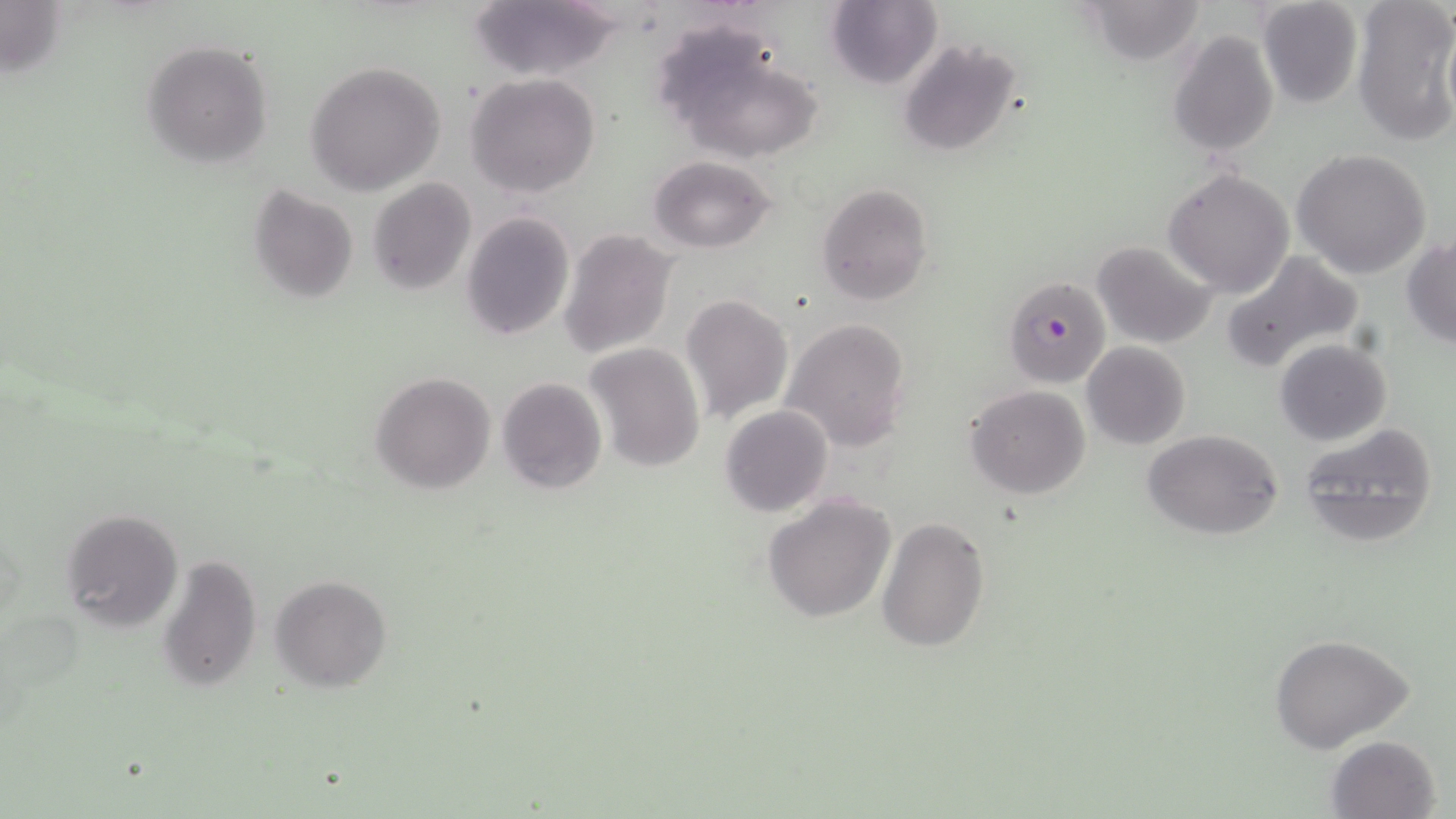
Plasmodium falciparum-infected red blood cell locations = approximate bounding boxes as named x1/y1/x2/y2 corners in pixels: (x1=1002, y1=277, x2=1111, y2=389)
slide-level diagnosis = Plasmodium falciparum
image size = 1456×819 pixels
field of view = one of a larger specimen
preparation = thin blood film
magnification = 1000x
modality = optical microscopy
stain = May-Grünwald-Giemsa
uninfected red blood cell locations = approximate bounding boxes as named x1/y1/x2/y2 corners in pixels: (x1=467, y1=0, x2=624, y2=82), (x1=1080, y1=0, x2=1209, y2=66), (x1=1352, y1=0, x2=1456, y2=147), (x1=826, y1=1, x2=943, y2=89), (x1=1257, y1=1, x2=1364, y2=109), (x1=651, y1=23, x2=824, y2=164), (x1=1168, y1=28, x2=1279, y2=156), (x1=896, y1=36, x2=1024, y2=157), (x1=140, y1=40, x2=273, y2=168), (x1=305, y1=60, x2=446, y2=195), (x1=466, y1=73, x2=600, y2=198), (x1=1293, y1=149, x2=1432, y2=280), (x1=650, y1=155, x2=776, y2=253), (x1=1163, y1=167, x2=1296, y2=298), (x1=367, y1=178, x2=477, y2=294), (x1=815, y1=182, x2=934, y2=306), (x1=248, y1=185, x2=359, y2=303), (x1=461, y1=211, x2=574, y2=340), (x1=559, y1=229, x2=677, y2=359), (x1=1403, y1=235, x2=1456, y2=346), (x1=1091, y1=239, x2=1217, y2=348), (x1=1219, y1=250, x2=1362, y2=375), (x1=680, y1=293, x2=794, y2=426), (x1=782, y1=317, x2=912, y2=452), (x1=1273, y1=339, x2=1392, y2=446), (x1=1082, y1=342, x2=1191, y2=450), (x1=585, y1=343, x2=706, y2=473), (x1=370, y1=372, x2=496, y2=494), (x1=496, y1=376, x2=608, y2=495), (x1=965, y1=385, x2=1092, y2=498), (x1=719, y1=404, x2=833, y2=517), (x1=1296, y1=421, x2=1441, y2=549), (x1=1141, y1=428, x2=1285, y2=541), (x1=760, y1=494, x2=898, y2=625), (x1=59, y1=507, x2=183, y2=633), (x1=878, y1=516, x2=989, y2=653), (x1=157, y1=553, x2=262, y2=691), (x1=270, y1=573, x2=393, y2=693), (x1=1271, y1=636, x2=1415, y2=754), (x1=1326, y1=735, x2=1442, y2=819)